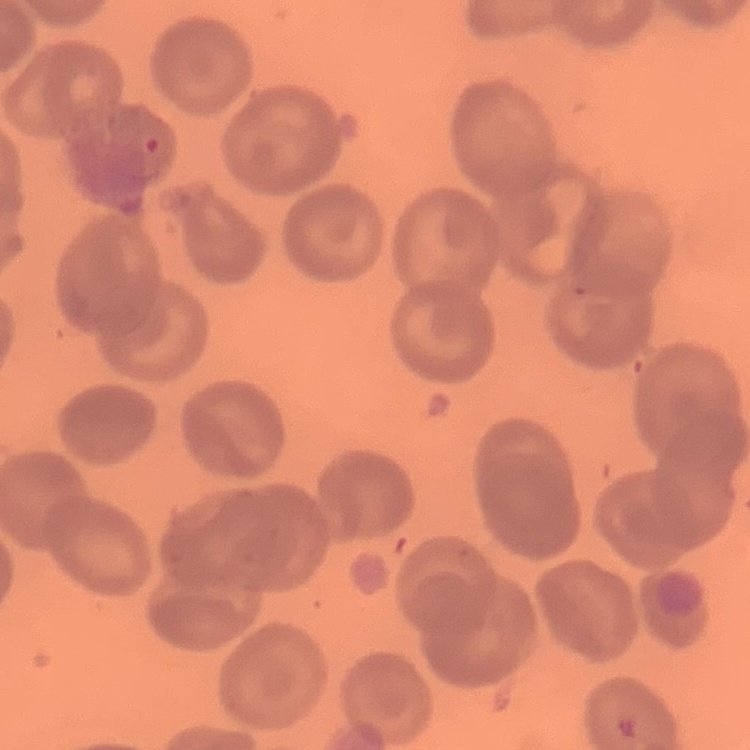
erythrocyte_morphology: no rouleaux formation
preparation: thin blood smear
stain: Field's or Giemsa
image_type: one tile cut from a larger photomicrograph